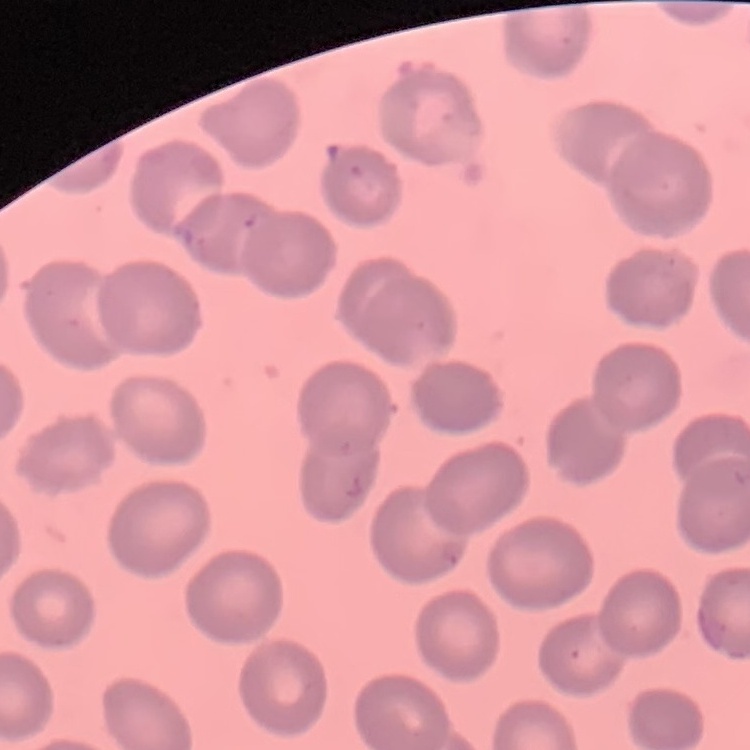

{
  "erythrocyte_morphology": "no rouleaux formation",
  "stain": "Field's or Giemsa",
  "preparation": "thin blood film",
  "image_type": "square crop of a larger photomicrograph"
}